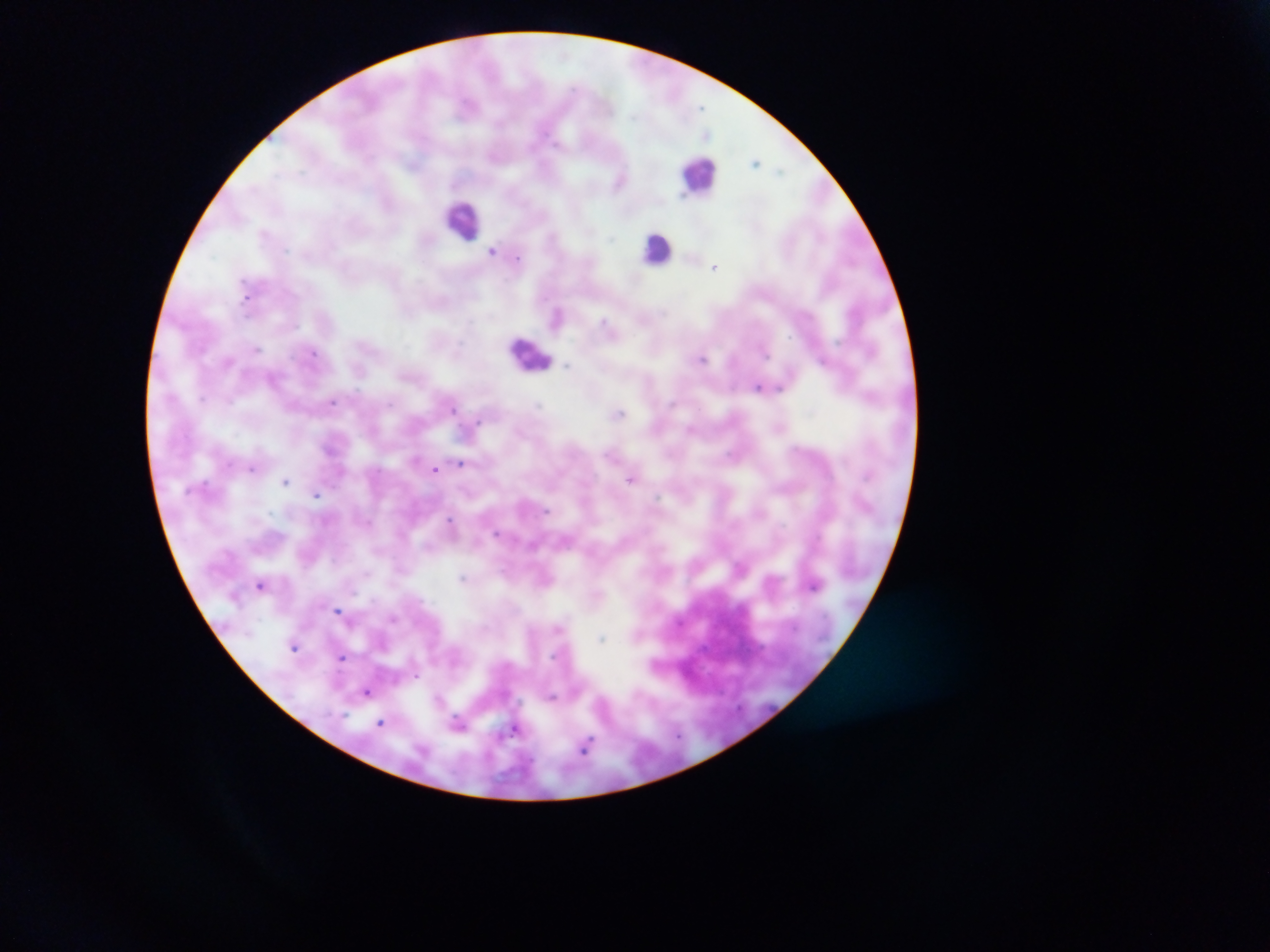
Approximate centers as [x, y] in pixels.
Summary:
  - Leukocyte locations: [700, 173], [462, 219], [656, 248], [532, 352]
  - Malaria parasite locations: [701, 107], [707, 134], [755, 161], [780, 171], [683, 197], [611, 238], [492, 251], [518, 257], [715, 267], [246, 298], [665, 313], [603, 321], [256, 349], [313, 352], [765, 353], [703, 359], [822, 360], [228, 361], [568, 365], [272, 378], [758, 386], [779, 388], [203, 398], [229, 401], [332, 402], [671, 403], [389, 404], [538, 405], [453, 408], [619, 413], [478, 421], [690, 428], [731, 456], [460, 462], [228, 463], [251, 469], [435, 469], [631, 479], [286, 481], [206, 484], [317, 495], [546, 511], [450, 519], [495, 533], [367, 573], [462, 577], [260, 584], [814, 586], [338, 610], [394, 618], [557, 628], [602, 638], [294, 647], [341, 657], [417, 677], [367, 693], [553, 697], [439, 698], [381, 723], [459, 723], [513, 730], [678, 735], [586, 745]
  - Preparation: thick blood smear
  - Image size: 1270×952 pixels
  - Capture: mobile-phone photograph through a microscope
  - Country: Ghana
  - Field of view: single